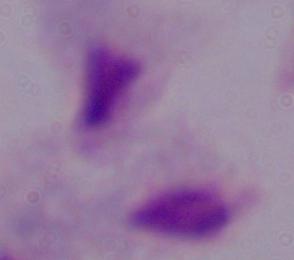

identification = trichomonad
modality = photomicrograph
magnification = 1000x